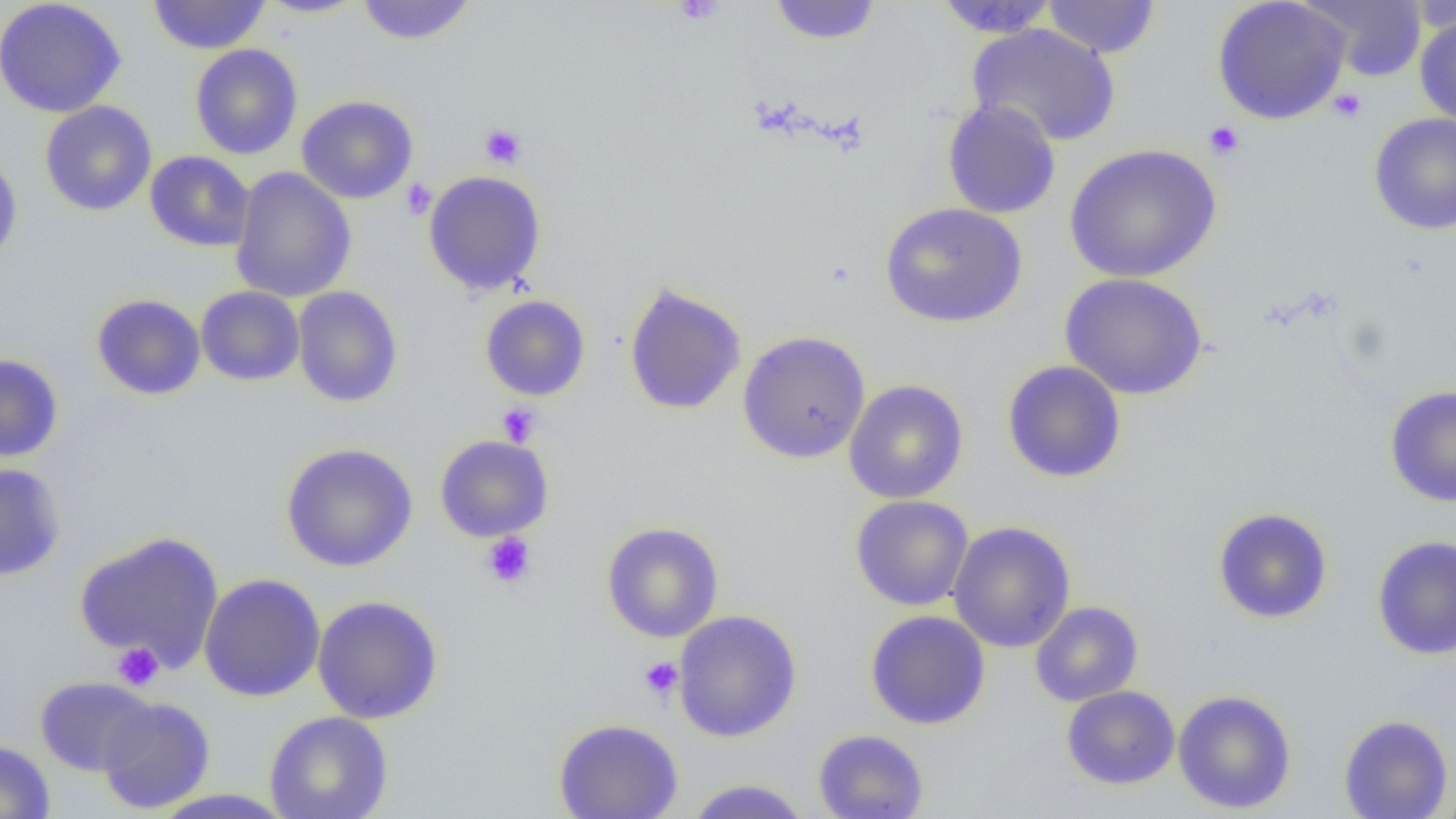
slide_level_diagnosis: negative for blood parasites
image_size: 1456×819 pixels
platelet_locations: 'approximate bounding boxes as [x1, y1, x2, y2] in pixels: [673, 0, 726, 25], [1328, 88, 1366, 123], [1204, 121, 1245, 160], [479, 123, 526, 169], [400, 178, 436, 220], [496, 403, 541, 447], [481, 532, 537, 589], [112, 642, 164, 690], [639, 657, 683, 700]'
field_of_view: one of a larger specimen
preparation: thin blood smear
magnification: 1000x
uninfected_red_blood_cell_locations: 'approximate bounding boxes as [x1, y1, x2, y2] in pixels: [0, 0, 127, 118], [147, 0, 270, 54], [256, 0, 368, 18], [357, 0, 476, 46], [768, 0, 882, 45], [934, 0, 1059, 38], [1042, 0, 1160, 58], [1212, 0, 1351, 125], [1303, 0, 1428, 82], [1414, 14, 1456, 128], [966, 23, 1121, 147], [190, 44, 303, 160], [297, 95, 419, 205], [942, 99, 1061, 219], [40, 101, 157, 216], [1369, 112, 1456, 235], [1064, 143, 1222, 283], [0, 150, 23, 269], [144, 151, 255, 252], [230, 167, 357, 303], [423, 170, 547, 296], [879, 203, 1027, 327], [1060, 273, 1208, 400], [623, 282, 747, 416], [195, 286, 305, 386], [292, 286, 403, 408], [91, 294, 206, 400], [479, 295, 591, 401], [737, 330, 871, 464], [0, 354, 64, 463], [1002, 360, 1127, 484], [843, 379, 969, 504], [1384, 385, 1456, 508], [434, 434, 554, 542], [280, 442, 419, 572], [0, 462, 66, 581], [850, 495, 974, 611], [1213, 507, 1333, 624], [948, 520, 1076, 653], [601, 522, 724, 643], [74, 530, 224, 672], [1372, 534, 1456, 659], [198, 573, 326, 702], [312, 595, 443, 724], [1029, 600, 1144, 707], [673, 610, 802, 742], [865, 610, 990, 730], [34, 676, 156, 776], [1061, 685, 1180, 790], [1172, 689, 1296, 814], [97, 696, 215, 814], [264, 710, 393, 819], [1338, 714, 1453, 819], [553, 717, 684, 819], [813, 729, 929, 819], [0, 740, 55, 819], [683, 778, 812, 819], [1433, 785, 1456, 818], [147, 789, 297, 818]'
modality: optical microscopy